Identify the parasite.
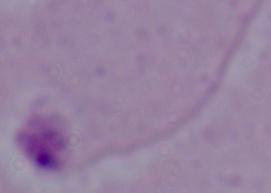

This is Leishmania.

Micrograph. Captured at 1000x magnification.